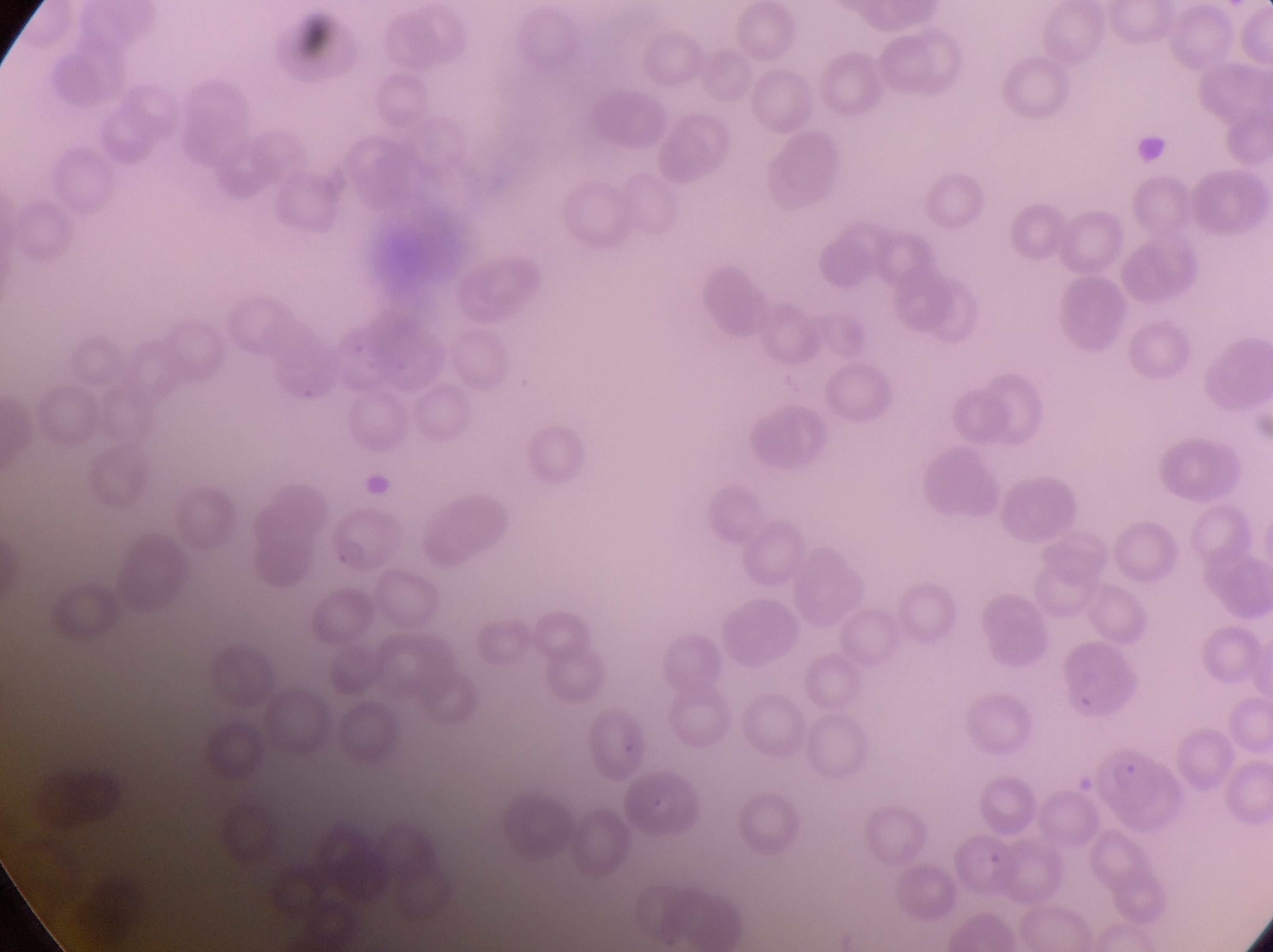
magnification: 1000x
image_size: 1273×952 pixels
country: Uganda
field_of_view: single
parasitised_red_blood_cell_locations: 'approximate bounding boxes as (left, top, right, bottom) in pixels: (327, 510, 402, 572), (1064, 645, 1143, 719), (1081, 739, 1191, 837), (627, 776, 710, 849), (956, 827, 1018, 899)'
capture: smartphone photograph through the eyepiece of an Olympus CX-23 microscope
artifact_platelet_like_body_stain_precipitate_or_debris_locations: 'approximate bounding boxes as (left, top, right, bottom) in pixels: (1131, 135, 1171, 178)'
preparation: thin blood smear